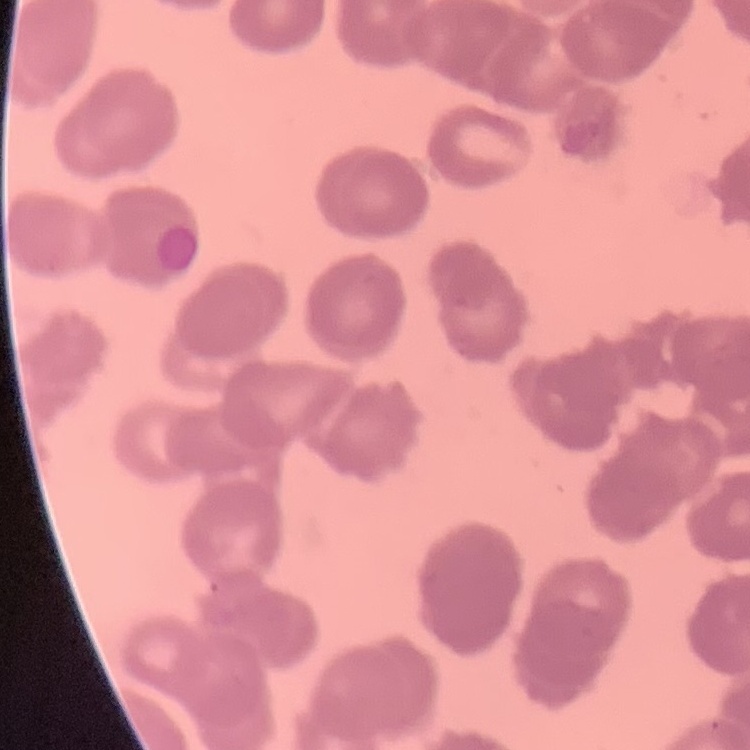 The erythrocytes show rouleaux formation. Thin blood smear. One tile cut from a larger photomicrograph. Stained with either Field's or Giemsa.